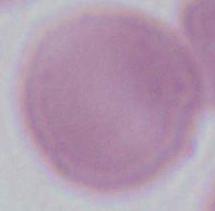

Summary:
  - Magnification: 1000x
  - Modality: photomicrograph
  - Identification: erythrocyte